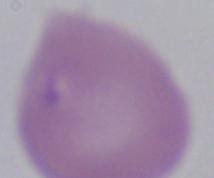

Summary:
  - Modality: micrograph
  - Magnification: 1000x
  - Identification: Babesia